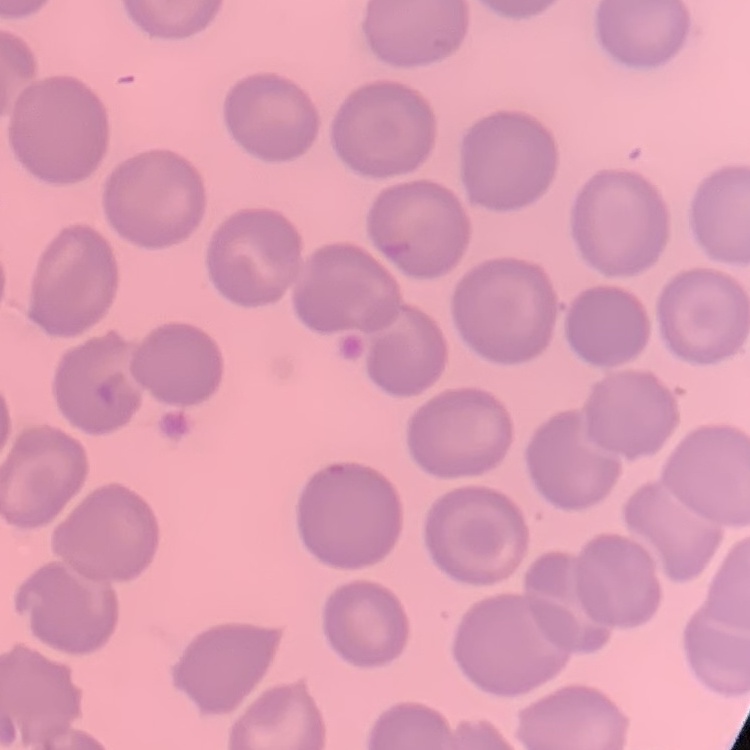

The erythrocytes exhibit no rouleaux formation. Stained with either Field's or Giemsa. Square crop of a larger photomicrograph. Thin blood smear.